Give the extent of the malaria parasites you find, grouped by life-cycle stage — ring form, trophozoite, schizont, or gametocyte.
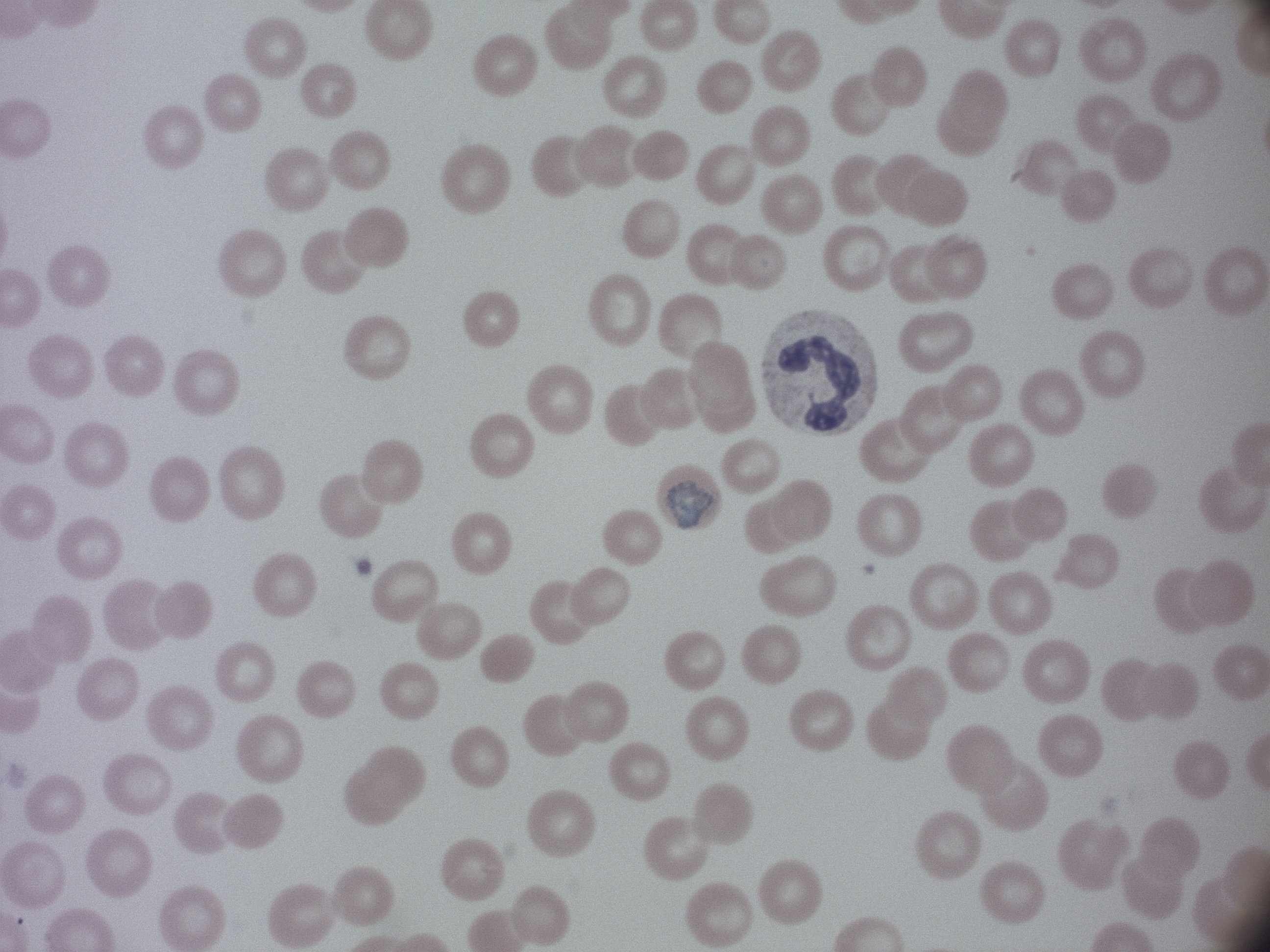

Approximate bounding boxes as [x1, y1, x2, y2] in pixels, from the source annotation, which is not necessarily exhaustive.
Gametocytes: [667, 480, 713, 530].

Species: Plasmodium malariae. Image is 1270×952 pixels. Captured at 100x magnification. Giemsa stain. Single field of view. Thin blood smear. Acquired with a Leica DM2000 optical microscope and its built-in camera.